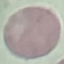

Malaria status: uninfected. Cell patch, automatically extracted from a larger field of view and resized to 64 × 64 pixels. Thin smear of blood. Acquired by smartphone through the microscope eyepiece. Giemsa-stained preparation.